Assess this cell for malaria.
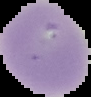

Uninfected.

From a thin blood smear. Segmented cell region on a black background. Image is 91×97 pixels.